Give the preparation type.
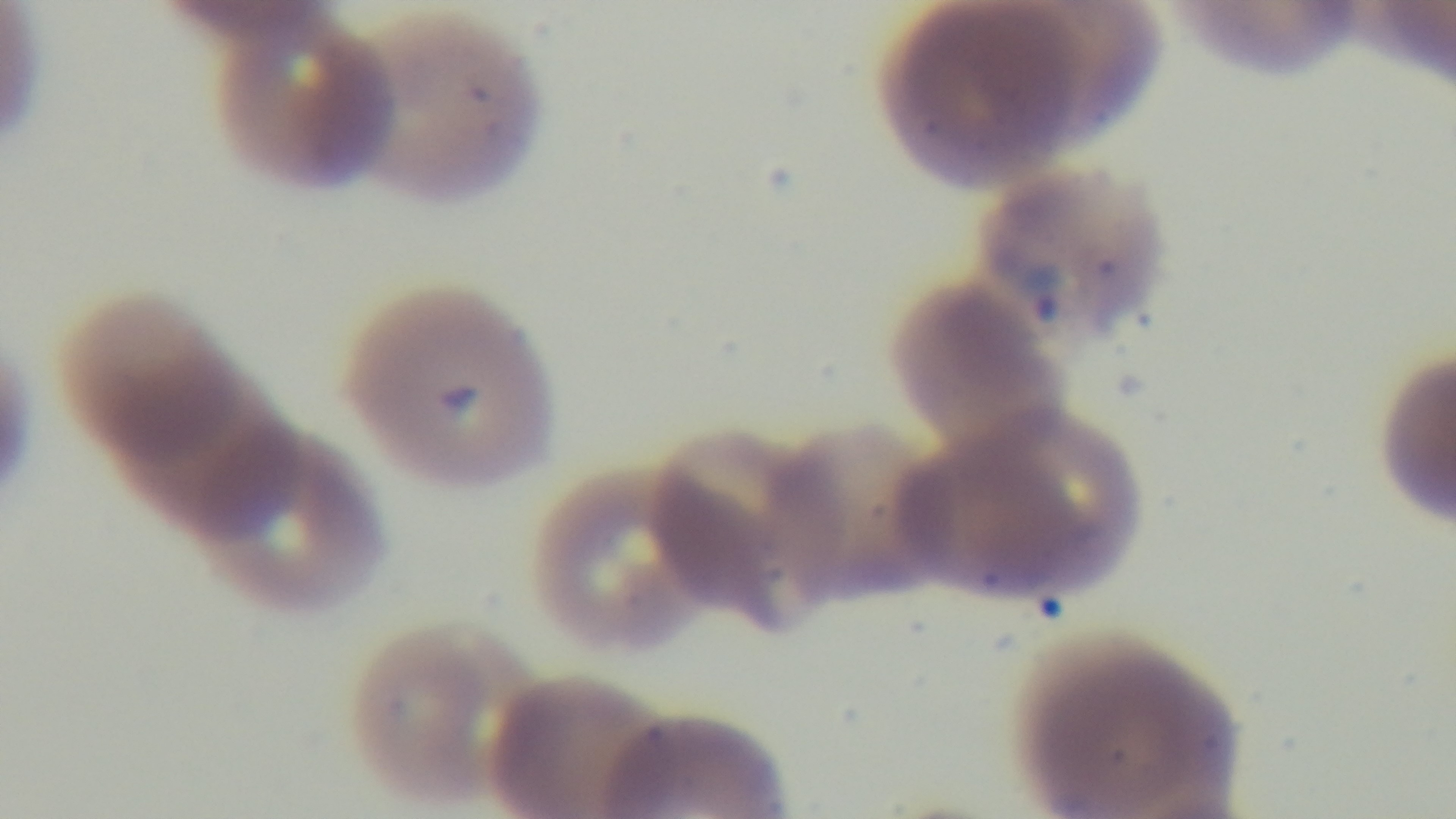
It is a thin blood film.

Light microscopy. Giemsa stain. Captured with a mounted 4K digital camera. 100x oil-immersion objective. Malaria status: positive. One field from the slide.